Assess this cell for malaria.
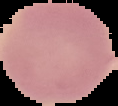

It is uninfected.

{
  "image_size": "118×106 pixels",
  "image_type": "segmented cell region with the area outside set to black",
  "preparation": "thin blood film"
}